Outline each blood parasite and name the species.
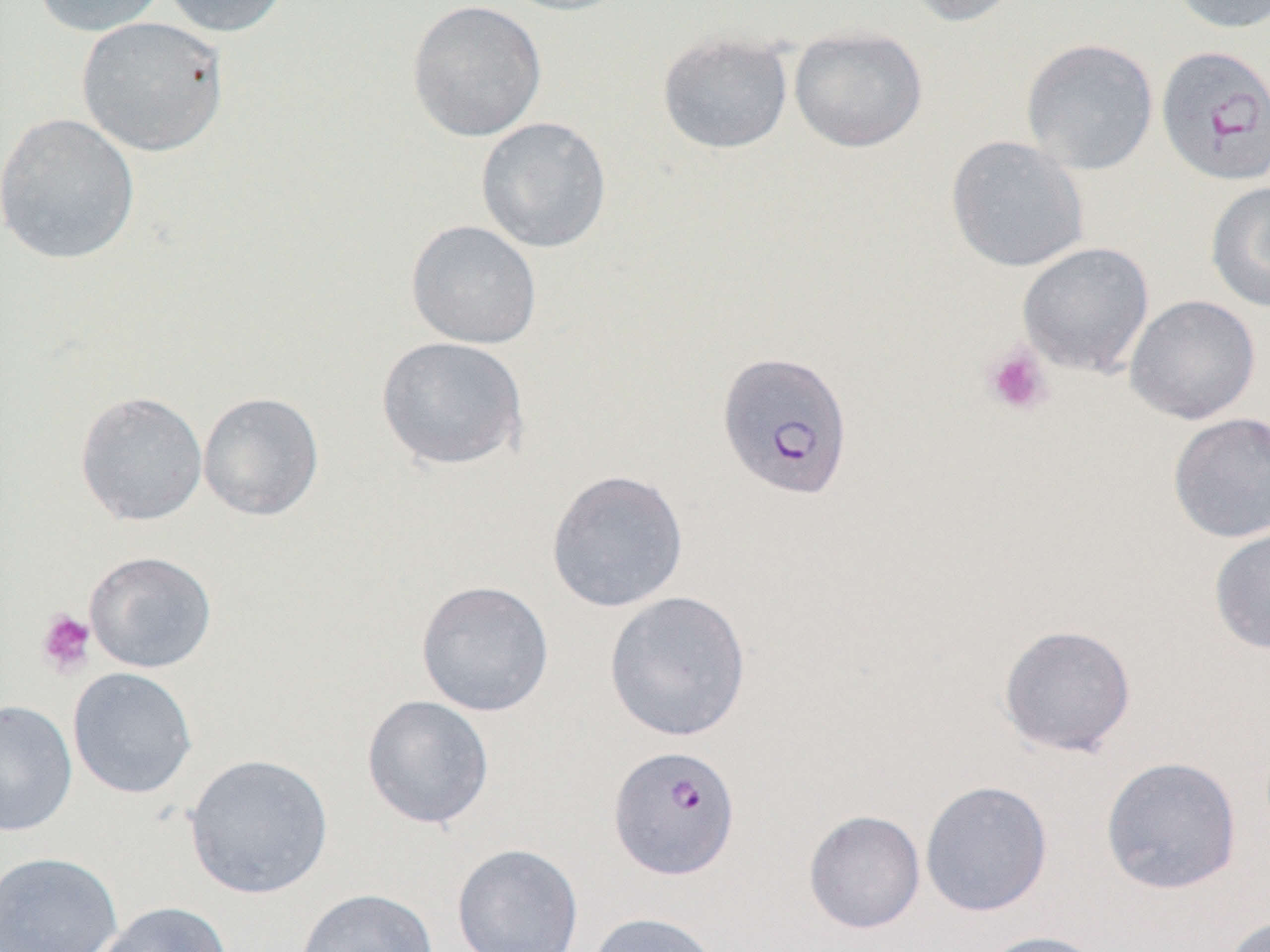

Approximate bounding boxes as (x1, y1, x2, y2) in pixels.
Plasmodium falciparum-infected red blood cells: (1155, 44, 1270, 187), (716, 350, 854, 502), (607, 744, 741, 880).
No Plasmodium ovale, Plasmodium malariae, Plasmodium vivax, Babesia divergens, or Trypanosoma brucei observed.

{
  "slide_level_diagnosis": "Plasmodium falciparum",
  "uninfected_red_blood_cell_locations": "approximate bounding boxes as (x1, y1, x2, y2) in pixels: (31, 0, 170, 37), (160, 0, 292, 38), (495, 0, 634, 16), (900, 0, 1026, 27), (1166, 0, 1270, 34), (406, 1, 547, 143), (75, 16, 229, 157), (788, 26, 928, 153), (657, 31, 794, 154), (1021, 37, 1159, 175), (0, 112, 142, 265), (475, 116, 612, 254), (946, 135, 1089, 272), (1205, 181, 1270, 314), (405, 219, 542, 349), (1017, 241, 1154, 378), (1125, 294, 1261, 425), (376, 336, 528, 471), (74, 390, 208, 526), (198, 391, 324, 522), (1167, 412, 1270, 543), (546, 469, 689, 613), (1208, 523, 1270, 656), (84, 550, 217, 673), (415, 579, 554, 717), (604, 590, 751, 742), (997, 623, 1137, 758), (67, 667, 197, 799), (361, 695, 495, 830), (0, 699, 78, 837), (183, 753, 334, 900), (1100, 756, 1243, 895), (919, 780, 1053, 917), (803, 809, 925, 934), (451, 843, 584, 952), (0, 851, 123, 952), (296, 887, 439, 952), (96, 901, 233, 952), (586, 911, 723, 952), (1221, 915, 1270, 952), (975, 929, 1109, 952)",
  "field_of_view": "one of a larger specimen",
  "preparation": "thin blood smear",
  "magnification": "1000x",
  "image_size": "1270×952 pixels",
  "modality": "optical microscopy",
  "platelet_locations": "approximate bounding boxes as (x1, y1, x2, y2) in pixels: (982, 344, 1053, 417), (36, 608, 96, 678)"
}